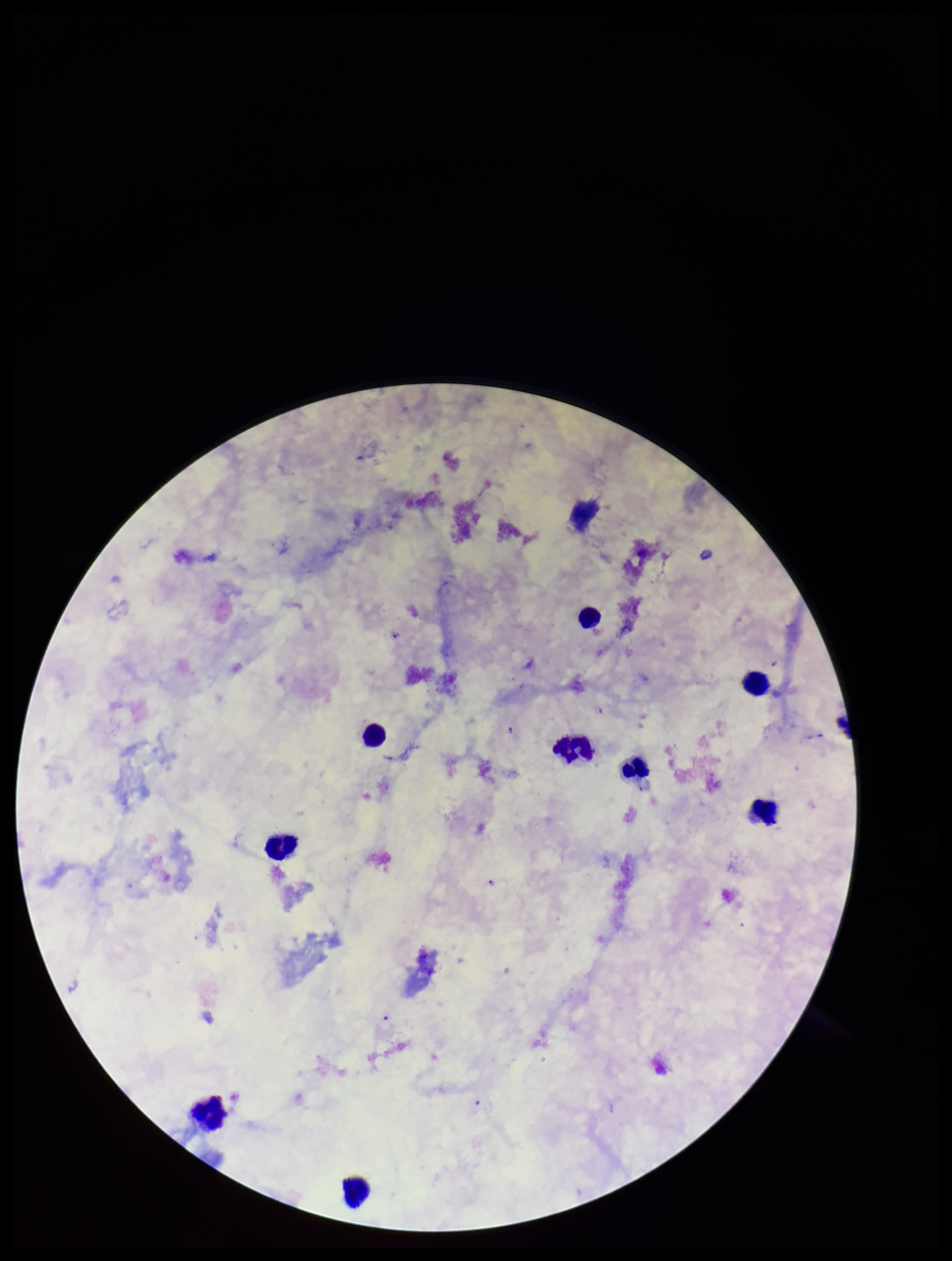

Summary:
  - Leukocyte count: 9
  - Plasmodium parasites: identified
  - Preparation: thick
  - Image size: 952×1261 pixels
  - Capture: smartphone photograph through the microscope eyepiece
  - Stain: Giemsa
  - Field of view: single
  - Parasite count: 4
  - Species reported for this patient: Plasmodium falciparum
  - Patient malaria status: infected